Assess this cell for malaria.
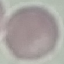
Uninfected.

{
  "capture": "smartphone through the microscope eyepiece",
  "image_type": "automatically extracted cell patch, resized to 64 × 64 pixels",
  "preparation": "thin blood smear",
  "stain": "Giemsa"
}